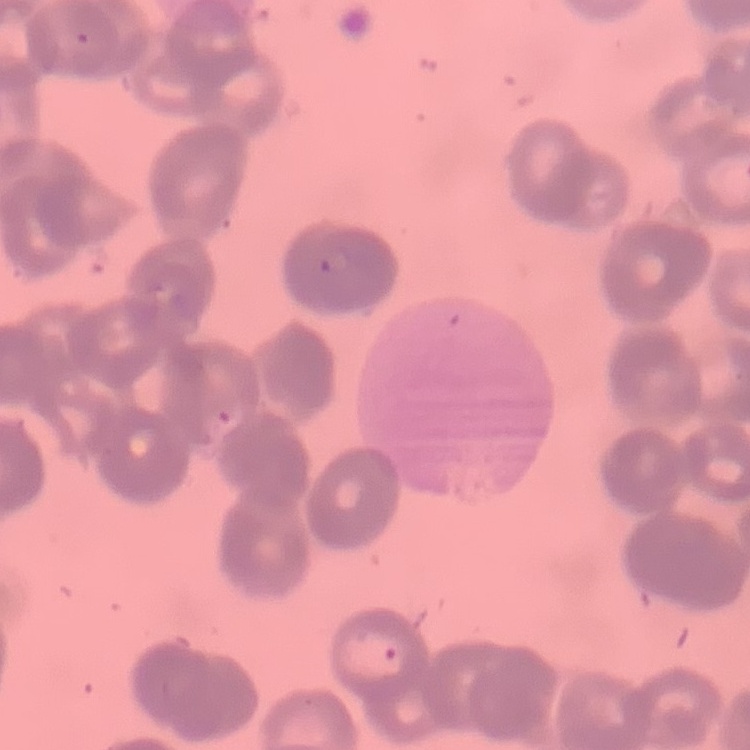

red blood cell morphology = rouleaux formation
preparation = thin blood smear
image type = square crop of a larger photomicrograph
stain = Field's or Giemsa